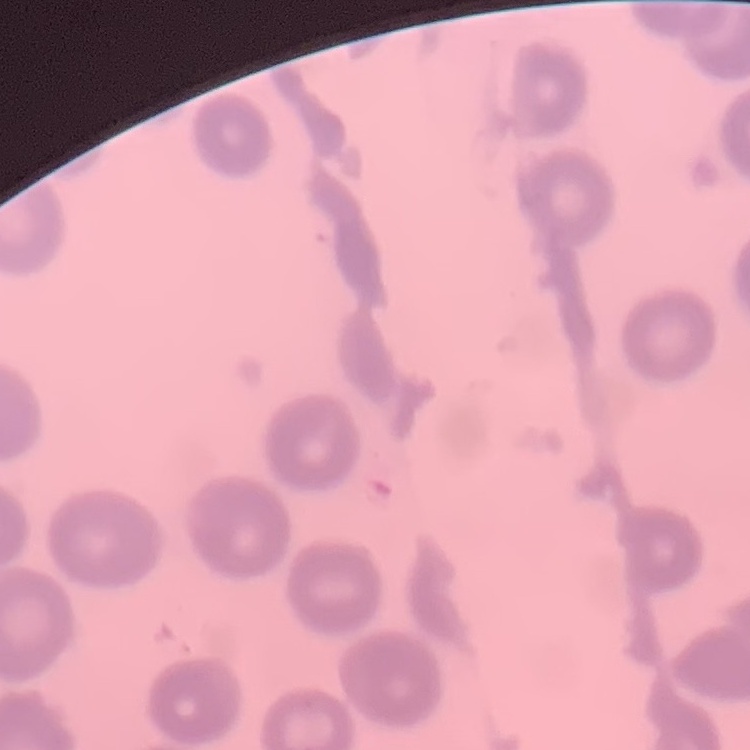
Summary:
  - Erythrocyte morphology: no rouleaux formation
  - Preparation: thin blood smear
  - Stain: Field's or Giemsa
  - Image type: square crop of a larger photomicrograph